Give the extent of all Trypanosoma brucei.
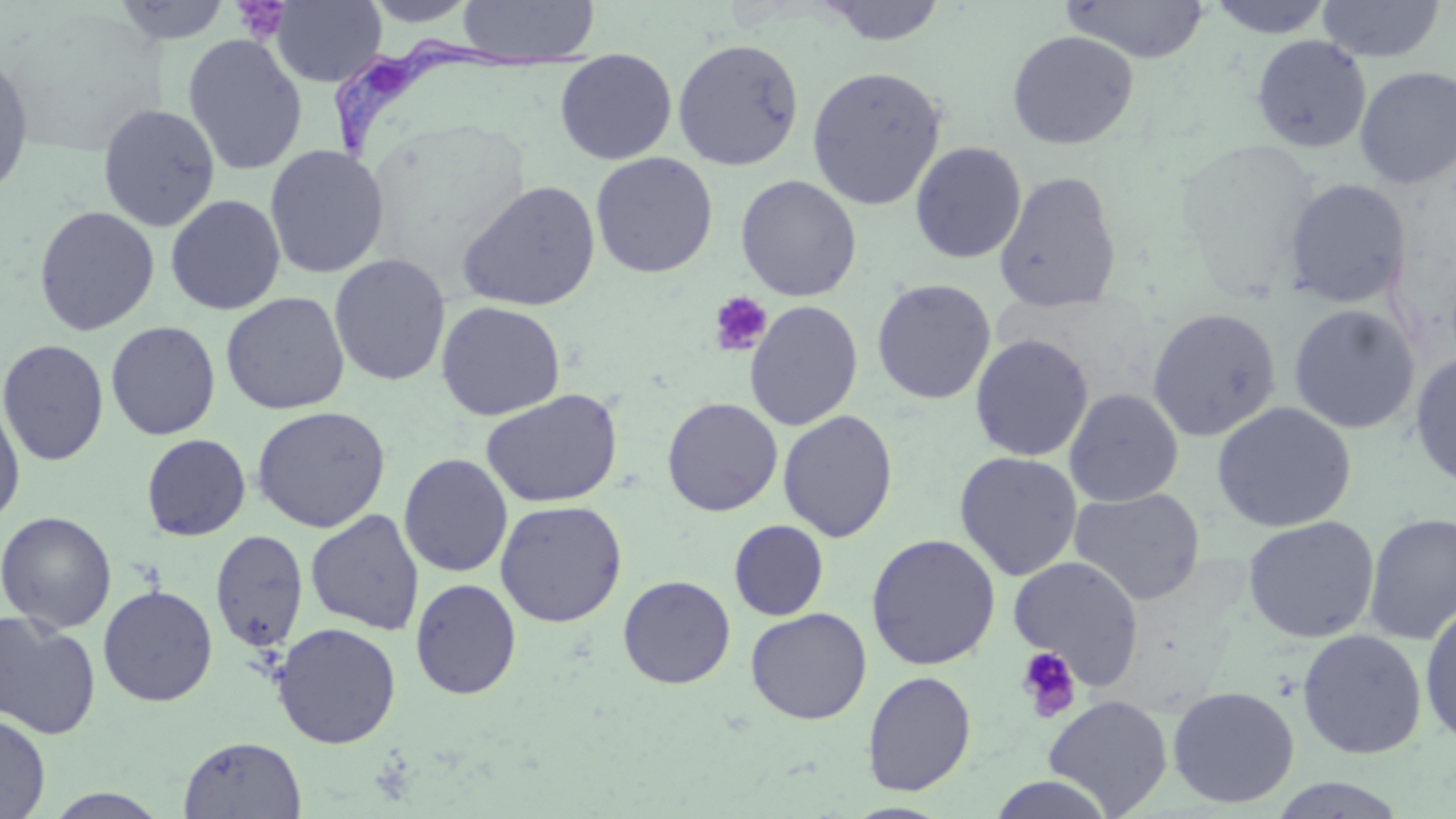

Approximate bounding boxes as (x1, y1, x2, y2) in pixels.
Trypanosoma brucei: (325, 37, 595, 177).

Uninfected red blood cell locations: (360, 0, 483, 27), (455, 0, 600, 63), (813, 0, 949, 46), (1060, 0, 1211, 63), (1206, 0, 1336, 38), (1316, 0, 1446, 63), (110, 1, 232, 44), (268, 1, 386, 87), (1006, 30, 1139, 150), (182, 33, 307, 176), (1251, 35, 1372, 154), (672, 37, 805, 170), (555, 50, 677, 164), (0, 51, 34, 199), (1354, 65, 1456, 189), (806, 66, 947, 210), (98, 103, 220, 232), (1175, 138, 1320, 290), (910, 141, 1027, 264), (264, 144, 389, 278), (590, 152, 718, 278), (994, 169, 1122, 313), (736, 174, 861, 301), (1283, 178, 1412, 308), (456, 180, 601, 311), (165, 194, 286, 315), (33, 205, 160, 336), (329, 253, 451, 387), (871, 279, 996, 405), (221, 291, 349, 415), (744, 300, 863, 431), (436, 301, 565, 421), (1288, 304, 1420, 435), (1146, 307, 1282, 442), (105, 320, 221, 441), (970, 333, 1094, 462), (0, 339, 109, 466), (1409, 352, 1456, 489), (480, 388, 624, 508), (1064, 388, 1184, 507), (0, 396, 26, 530), (662, 397, 783, 516), (1211, 401, 1357, 533), (252, 405, 391, 533), (777, 410, 898, 542), (141, 433, 251, 541), (954, 451, 1083, 581), (398, 453, 513, 578), (1069, 487, 1206, 605), (494, 499, 627, 627), (306, 509, 425, 635), (1, 511, 116, 633), (1363, 512, 1456, 645), (1242, 515, 1381, 643), (729, 520, 829, 621), (210, 529, 308, 652), (865, 534, 1001, 671), (1008, 554, 1145, 687), (618, 575, 736, 689), (411, 578, 521, 699), (98, 585, 218, 707), (1420, 601, 1456, 747), (745, 607, 871, 724), (0, 609, 101, 740), (272, 622, 401, 749), (1297, 629, 1427, 759), (862, 670, 976, 796), (1166, 685, 1300, 808), (1043, 694, 1173, 816), (0, 712, 51, 819), (178, 736, 307, 818), (985, 775, 1118, 819), (1268, 776, 1411, 818). Platelet locations: (233, 1, 291, 44), (708, 291, 773, 356), (1015, 646, 1081, 721). Slide-level diagnosis: Trypanosoma brucei. May-Grünwald-Giemsa-stained preparation. Single field of view. Image is 1456×819 pixels. Thin blood smear. Captured at 1000x magnification. Optical microscopy.